Identify the parasite.
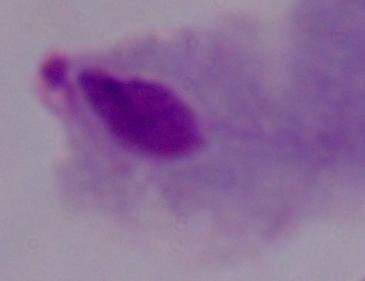

A trichomonad.

Photomicrograph. Captured at 1000x magnification.